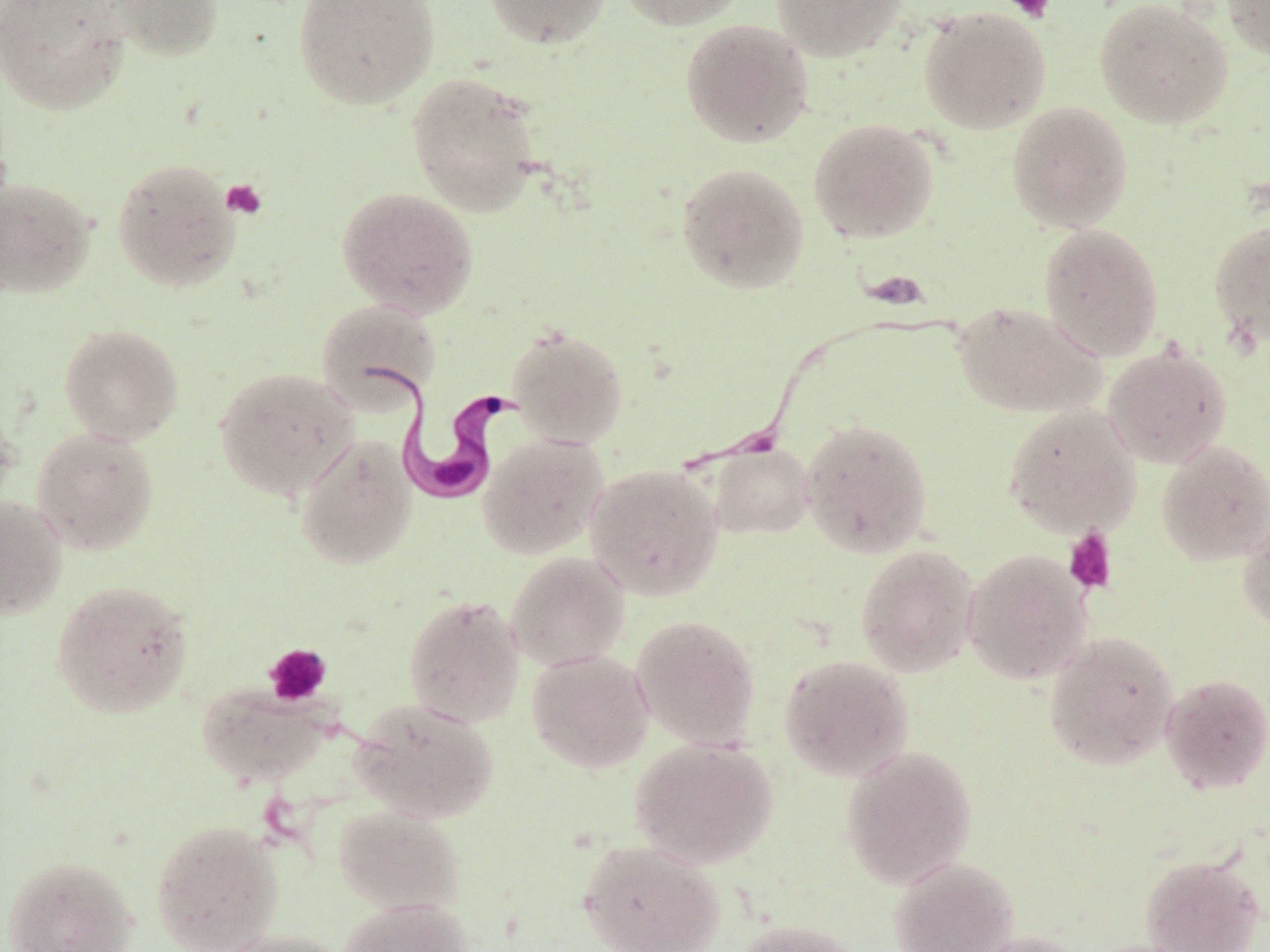

{
  "slide_level_diagnosis": "Trypanosoma brucei",
  "image_size": "1270×952 pixels",
  "magnification": "1000x",
  "uninfected_red_blood_cell_locations": "approximate bounding boxes as (x1, y1, x2, y2) in pixels: (0, 0, 131, 114), (102, 0, 224, 62), (293, 0, 439, 110), (482, 0, 611, 48), (616, 0, 749, 31), (771, 0, 908, 62), (1222, 0, 1270, 61), (1094, 1, 1234, 130), (918, 6, 1052, 135), (679, 18, 814, 150), (406, 72, 542, 217), (1005, 100, 1134, 234), (807, 117, 940, 244), (111, 157, 241, 292), (675, 162, 810, 294), (0, 176, 97, 299), (336, 187, 478, 317), (1207, 219, 1270, 347), (1038, 222, 1164, 361), (316, 298, 442, 413), (950, 300, 1106, 419), (58, 323, 185, 445), (506, 325, 629, 449), (1103, 342, 1232, 469), (213, 366, 359, 501), (0, 398, 21, 517), (1003, 405, 1141, 538), (800, 417, 934, 559), (31, 427, 159, 556), (295, 434, 417, 571), (477, 434, 608, 559), (1157, 440, 1270, 566), (707, 442, 814, 540), (585, 463, 725, 600), (0, 495, 68, 620), (1237, 514, 1270, 637), (855, 544, 980, 677), (961, 548, 1093, 685), (506, 552, 630, 671), (50, 579, 194, 719), (403, 594, 525, 727), (630, 614, 761, 750), (1043, 630, 1180, 771), (526, 649, 654, 773), (779, 654, 914, 781), (1159, 673, 1270, 794), (196, 683, 331, 788), (347, 697, 500, 824), (629, 737, 778, 869), (841, 745, 978, 888), (332, 804, 466, 916), (150, 818, 285, 952), (576, 837, 727, 952), (2, 854, 139, 952), (1140, 854, 1264, 952), (888, 855, 1019, 952), (337, 898, 474, 952), (732, 918, 866, 952), (215, 927, 353, 952), (969, 930, 1088, 952)",
  "trypanosoma_brucei_locations": "approximate bounding boxes as (x1, y1, x2, y2) in pixels: (368, 364, 516, 508)",
  "platelet_locations": "approximate bounding boxes as (x1, y1, x2, y2) in pixels: (1004, 0, 1056, 22), (221, 179, 268, 219), (1063, 526, 1118, 595), (263, 643, 331, 707)",
  "field_of_view": "one of a larger specimen",
  "stain": "May-Grünwald-Giemsa",
  "preparation": "thin blood film",
  "modality": "optical microscopy"
}